Classify this cell by malaria status.
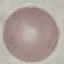
It is uninfected.

Thin blood film. Giemsa stain. Photographed with a smartphone camera at the microscope eyepiece. Cell patch, automatically extracted from a larger field of view and resized to 64 × 64 pixels.